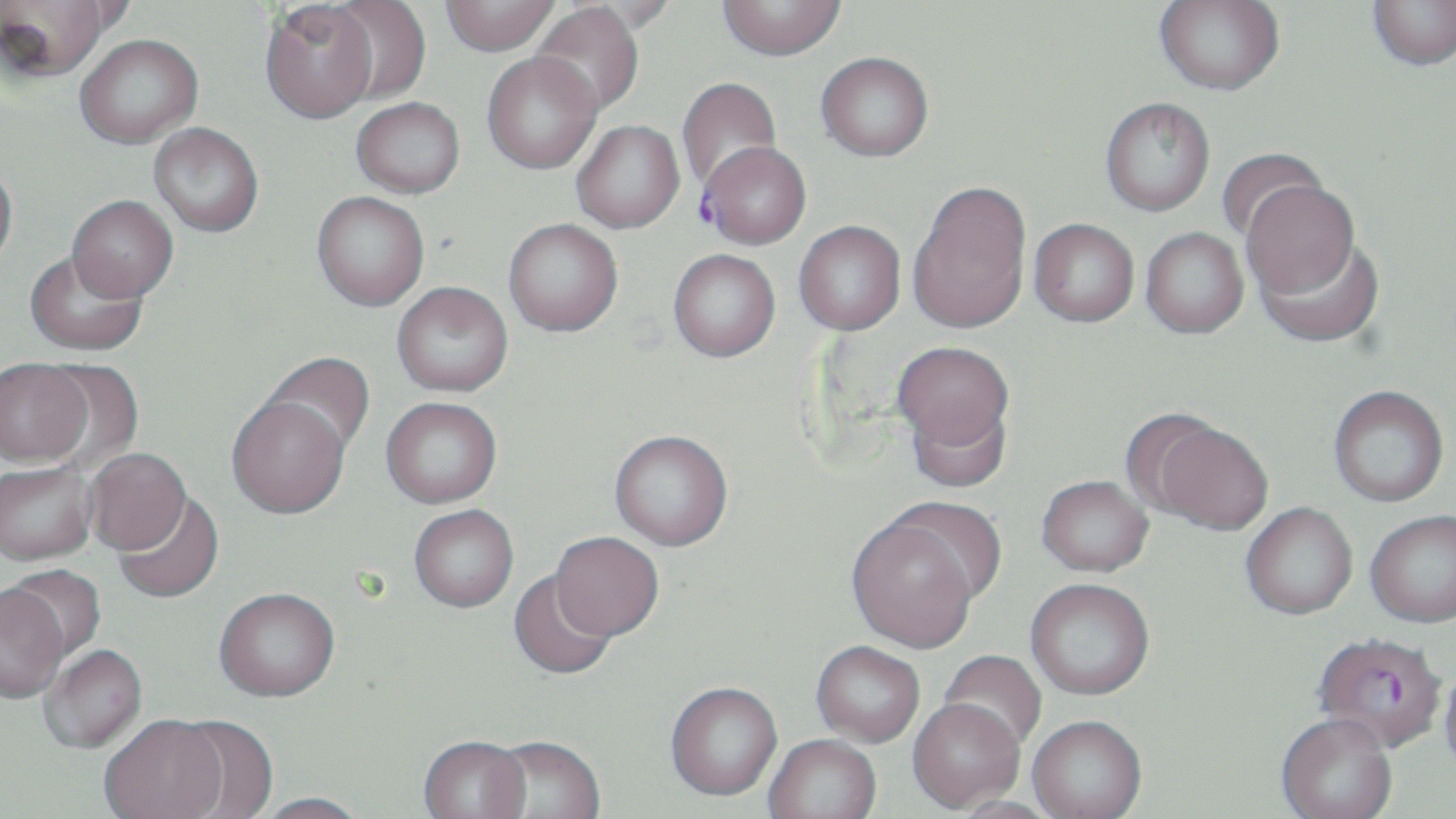
Summary:
  - Coordinate format: approximate bounding boxes as [x1, y1, x2, y2] in pixels
  - Uninfected red blood cell locations: [1, 0, 112, 82], [441, 0, 560, 56], [1368, 0, 1456, 70], [324, 1, 432, 104], [565, 1, 682, 35], [717, 1, 847, 60], [1154, 1, 1284, 95], [260, 2, 378, 124], [530, 3, 644, 118], [75, 34, 202, 148], [816, 52, 933, 161], [482, 53, 602, 174], [676, 77, 781, 195], [351, 97, 465, 198], [1100, 97, 1215, 216], [571, 120, 684, 233], [149, 123, 264, 236], [1215, 148, 1326, 245], [0, 159, 18, 272], [908, 180, 1032, 335], [1242, 180, 1361, 301], [312, 192, 429, 310], [67, 195, 178, 301], [503, 218, 623, 336], [1029, 218, 1139, 327], [793, 220, 906, 336], [1141, 227, 1248, 338], [1257, 232, 1384, 347], [667, 249, 780, 362], [25, 250, 148, 356], [392, 281, 512, 396], [892, 341, 1014, 456], [259, 351, 375, 458], [39, 360, 144, 469], [0, 361, 94, 469], [1328, 385, 1449, 507], [226, 396, 349, 520], [903, 396, 1013, 493], [380, 397, 502, 509], [1148, 419, 1274, 535], [609, 429, 733, 550], [84, 449, 192, 558], [0, 464, 97, 569], [1036, 475, 1154, 577], [115, 492, 225, 605], [1241, 502, 1358, 621], [409, 507, 518, 615], [1366, 510, 1456, 628], [847, 514, 981, 654], [549, 532, 664, 643], [4, 564, 106, 667], [508, 571, 617, 681], [1025, 578, 1155, 701], [0, 586, 70, 706], [214, 592, 340, 706], [811, 642, 925, 747], [40, 646, 148, 755], [938, 650, 1046, 753], [1439, 663, 1456, 779], [665, 684, 782, 804], [908, 701, 1024, 814], [168, 717, 279, 818], [1276, 717, 1397, 819], [100, 718, 229, 819], [1027, 718, 1148, 819], [764, 736, 882, 819], [487, 738, 605, 819], [417, 739, 532, 819], [252, 794, 371, 819], [948, 797, 1062, 819]
  - Plasmodium falciparum-infected red blood cell locations: [698, 141, 811, 250], [1313, 634, 1447, 756]
  - Slide-level diagnosis: Plasmodium falciparum
  - Preparation: thin blood film
  - Modality: optical microscopy
  - Image size: 1456×819 pixels
  - Magnification: 1000x
  - Field of view: one of a larger specimen
  - Stain: May-Grünwald-Giemsa